Outline each blood parasite and name the species.
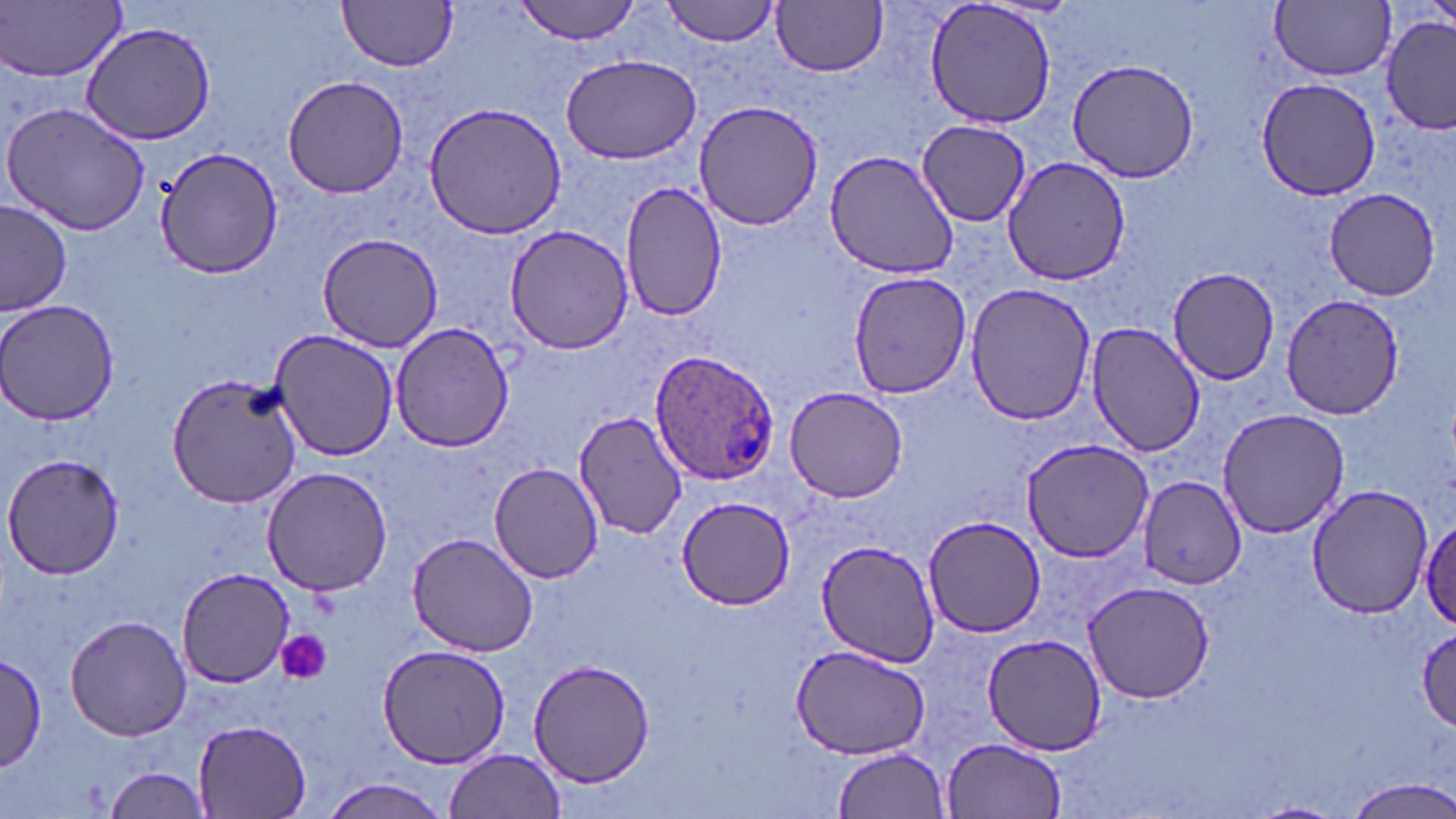

Approximate bounding boxes as named x1/y1/x2/y2 corners in pixels.
Plasmodium ovale-infected red blood cells: (x1=647, y1=348, x2=783, y2=487).
No Plasmodium falciparum, Plasmodium malariae, Plasmodium vivax, Babesia divergens, or Trypanosoma brucei observed.

Summary:
  - Platelet locations: (x1=274, y1=631, x2=332, y2=685)
  - Uninfected red blood cell locations: (x1=337, y1=0, x2=459, y2=72), (x1=515, y1=0, x2=644, y2=44), (x1=922, y1=0, x2=1062, y2=132), (x1=1272, y1=0, x2=1395, y2=81), (x1=2, y1=1, x2=127, y2=81), (x1=662, y1=1, x2=782, y2=45), (x1=773, y1=2, x2=888, y2=77), (x1=1381, y1=16, x2=1454, y2=133), (x1=78, y1=22, x2=221, y2=145), (x1=560, y1=53, x2=701, y2=164), (x1=1066, y1=59, x2=1201, y2=184), (x1=282, y1=74, x2=408, y2=198), (x1=1256, y1=78, x2=1382, y2=202), (x1=421, y1=100, x2=570, y2=239), (x1=693, y1=100, x2=822, y2=230), (x1=4, y1=102, x2=152, y2=236), (x1=917, y1=119, x2=1032, y2=226), (x1=155, y1=146, x2=281, y2=281), (x1=824, y1=149, x2=964, y2=280), (x1=1002, y1=155, x2=1132, y2=285), (x1=621, y1=180, x2=727, y2=323), (x1=1324, y1=187, x2=1442, y2=300), (x1=1, y1=199, x2=74, y2=316), (x1=504, y1=225, x2=637, y2=355), (x1=317, y1=231, x2=445, y2=353), (x1=846, y1=269, x2=972, y2=400), (x1=1170, y1=269, x2=1281, y2=385), (x1=963, y1=282, x2=1097, y2=426), (x1=1282, y1=293, x2=1405, y2=419), (x1=2, y1=300, x2=118, y2=428), (x1=1085, y1=320, x2=1205, y2=458), (x1=391, y1=322, x2=514, y2=453), (x1=268, y1=329, x2=400, y2=463), (x1=166, y1=371, x2=303, y2=508), (x1=783, y1=387, x2=909, y2=502), (x1=1216, y1=407, x2=1352, y2=539), (x1=572, y1=410, x2=689, y2=540), (x1=1021, y1=437, x2=1154, y2=563), (x1=3, y1=454, x2=125, y2=579), (x1=488, y1=461, x2=604, y2=585), (x1=262, y1=466, x2=393, y2=596), (x1=1137, y1=475, x2=1245, y2=588), (x1=1305, y1=485, x2=1435, y2=619), (x1=674, y1=496, x2=794, y2=609), (x1=1420, y1=515, x2=1456, y2=632), (x1=921, y1=516, x2=1049, y2=638), (x1=407, y1=531, x2=538, y2=658), (x1=816, y1=539, x2=941, y2=665), (x1=176, y1=568, x2=294, y2=688), (x1=1082, y1=578, x2=1218, y2=703), (x1=65, y1=614, x2=191, y2=741), (x1=1414, y1=626, x2=1456, y2=731), (x1=985, y1=636, x2=1106, y2=754), (x1=378, y1=644, x2=511, y2=770), (x1=790, y1=644, x2=931, y2=759), (x1=1, y1=652, x2=48, y2=771), (x1=528, y1=660, x2=657, y2=788), (x1=192, y1=719, x2=313, y2=817), (x1=944, y1=736, x2=1067, y2=818), (x1=445, y1=747, x2=567, y2=819), (x1=830, y1=747, x2=951, y2=819), (x1=103, y1=768, x2=212, y2=817), (x1=319, y1=776, x2=452, y2=818), (x1=1340, y1=777, x2=1456, y2=819)
  - Slide-level diagnosis: Plasmodium ovale
  - Magnification: 1000x
  - Field of view: single
  - Image size: 1456×819 pixels
  - Modality: light microscopy
  - Stain: May-Grünwald-Giemsa
  - Preparation: thin blood film